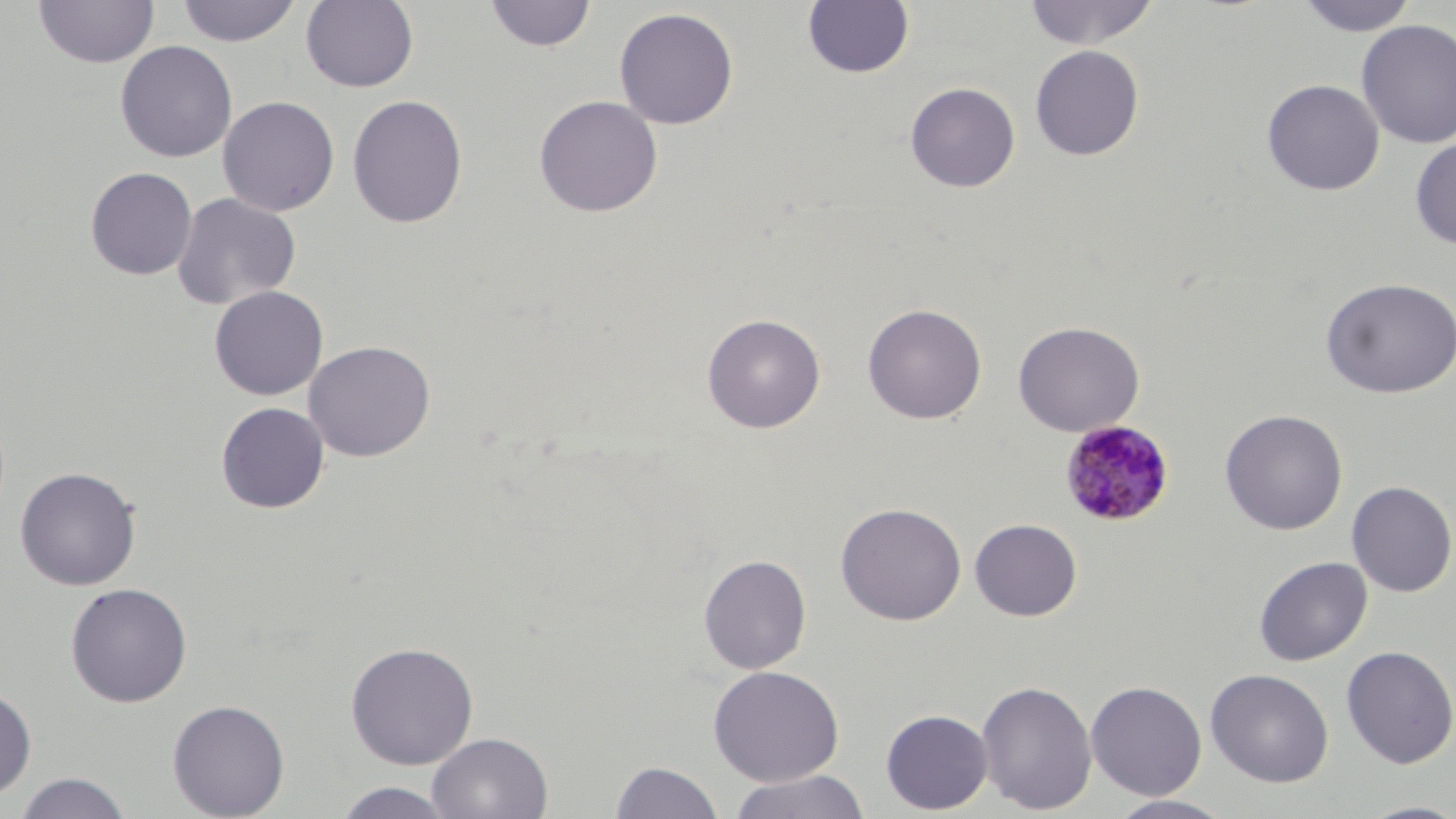
Summary:
  - Coordinate format: approximate bounding boxes as (x1,y1)-(x2,y2) corner pairs in pixels
  - Plasmodium malariae-infected red blood cell locations: (1059,419)-(1176,528)
  - Uninfected red blood cell locations: (175,0)-(303,47), (1023,0)-(1159,49), (1294,0)-(1420,37), (32,1)-(159,70), (300,1)-(419,93), (484,1)-(597,52), (802,1)-(915,79), (613,7)-(739,130), (1355,19)-(1456,149), (115,41)-(237,162), (1030,44)-(1145,160), (1261,79)-(1384,196), (905,81)-(1020,193), (347,94)-(468,228), (533,95)-(663,217), (217,96)-(340,217), (1410,137)-(1456,249), (84,167)-(198,280), (172,192)-(301,309), (1319,277)-(1456,399), (209,285)-(329,400), (862,303)-(987,424), (702,313)-(826,434), (1012,320)-(1145,436), (303,340)-(436,462), (215,401)-(330,514), (1219,409)-(1348,535), (14,466)-(142,591), (1346,480)-(1456,598), (835,501)-(967,626), (969,518)-(1082,621), (698,553)-(812,674), (1254,556)-(1373,666), (65,582)-(193,707), (344,641)-(479,769), (1340,645)-(1456,769), (708,665)-(845,786), (1205,668)-(1334,787), (976,679)-(1098,815), (1085,680)-(1207,800), (0,685)-(37,801), (167,699)-(290,818), (880,708)-(993,814), (427,732)-(553,818), (610,760)-(725,819), (727,770)-(871,819), (12,772)-(133,819), (332,781)-(457,818), (1106,794)-(1237,819), (1354,800)-(1456,819)
  - Slide-level diagnosis: Plasmodium malariae
  - Preparation: thin blood smear
  - Modality: optical microscopy
  - Stain: May-Grünwald-Giemsa
  - Magnification: 1000x
  - Image size: 1456×819 pixels
  - Field of view: single